Give the position of every leukocyte visible.
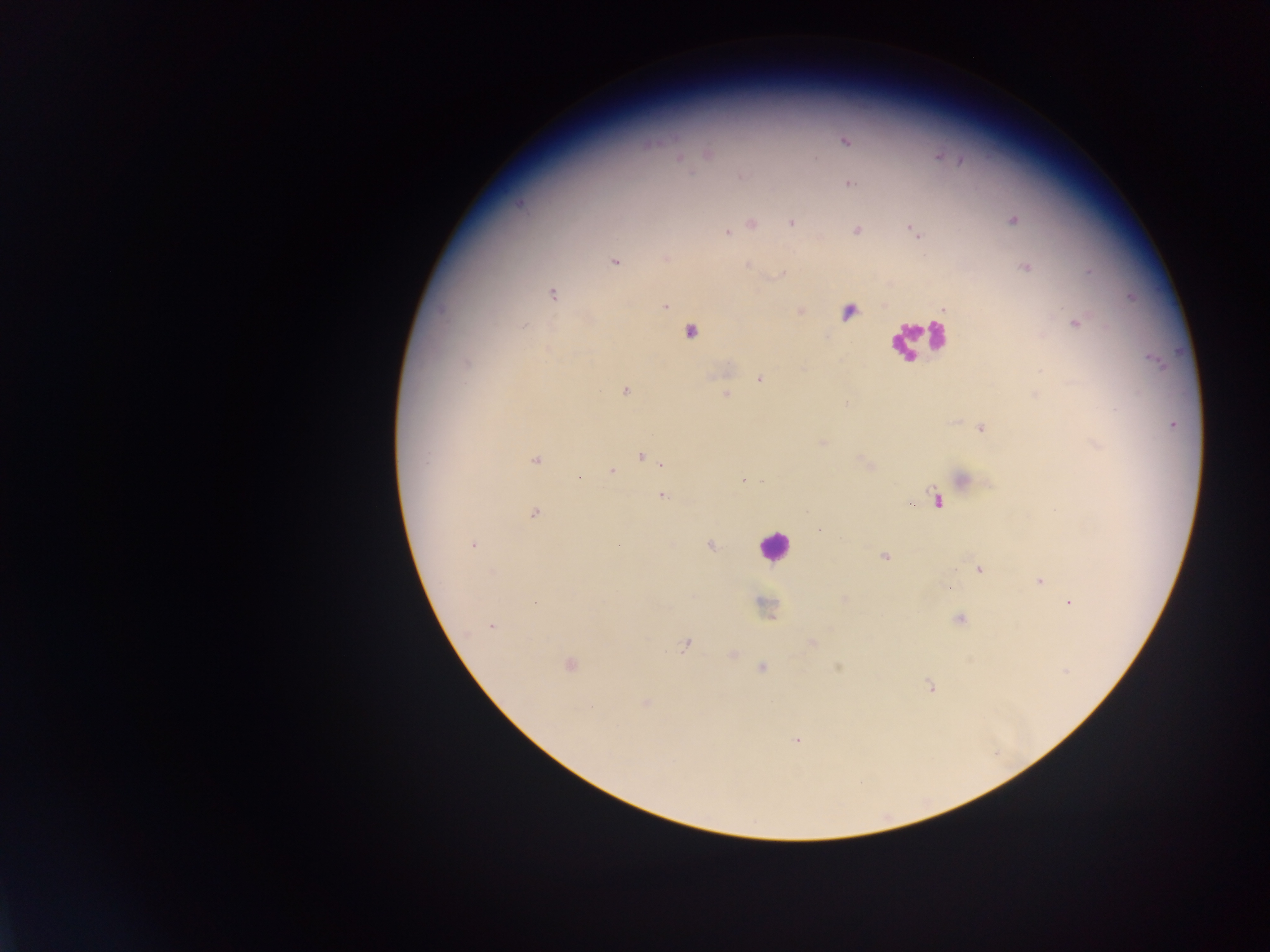

Approximate centers as (x, y) in pixels.
Leukocytes (some below the resolvable threshold): (690, 336), (915, 337), (773, 546).

Malaria parasite locations: (845, 142), (709, 154), (680, 157), (741, 176), (850, 184), (1013, 220), (792, 223), (752, 224), (913, 230), (857, 231), (726, 232), (665, 257), (615, 262), (748, 266), (1025, 267), (1090, 271), (782, 275), (553, 295), (665, 306), (800, 311), (848, 312), (1076, 324), (524, 326), (466, 363), (759, 379), (625, 391), (726, 395), (1173, 425), (981, 429), (822, 443), (1097, 446), (641, 456), (426, 457), (536, 460), (656, 461), (866, 463), (664, 464), (611, 470), (579, 477), (964, 479), (742, 481), (762, 482), (661, 495), (936, 500), (535, 513), (820, 530), (473, 544), (710, 546), (885, 556), (979, 570), (492, 572), (1040, 580), (1070, 603), (765, 606), (959, 620), (492, 626), (812, 643), (685, 644), (733, 655), (569, 664), (838, 667), (762, 668), (930, 685), (645, 704), (591, 707), (797, 740). Mobile-phone photograph taken through the microscope. One field of view. Thick blood smear. Sample from Ghana. Image is 1270×952 pixels.